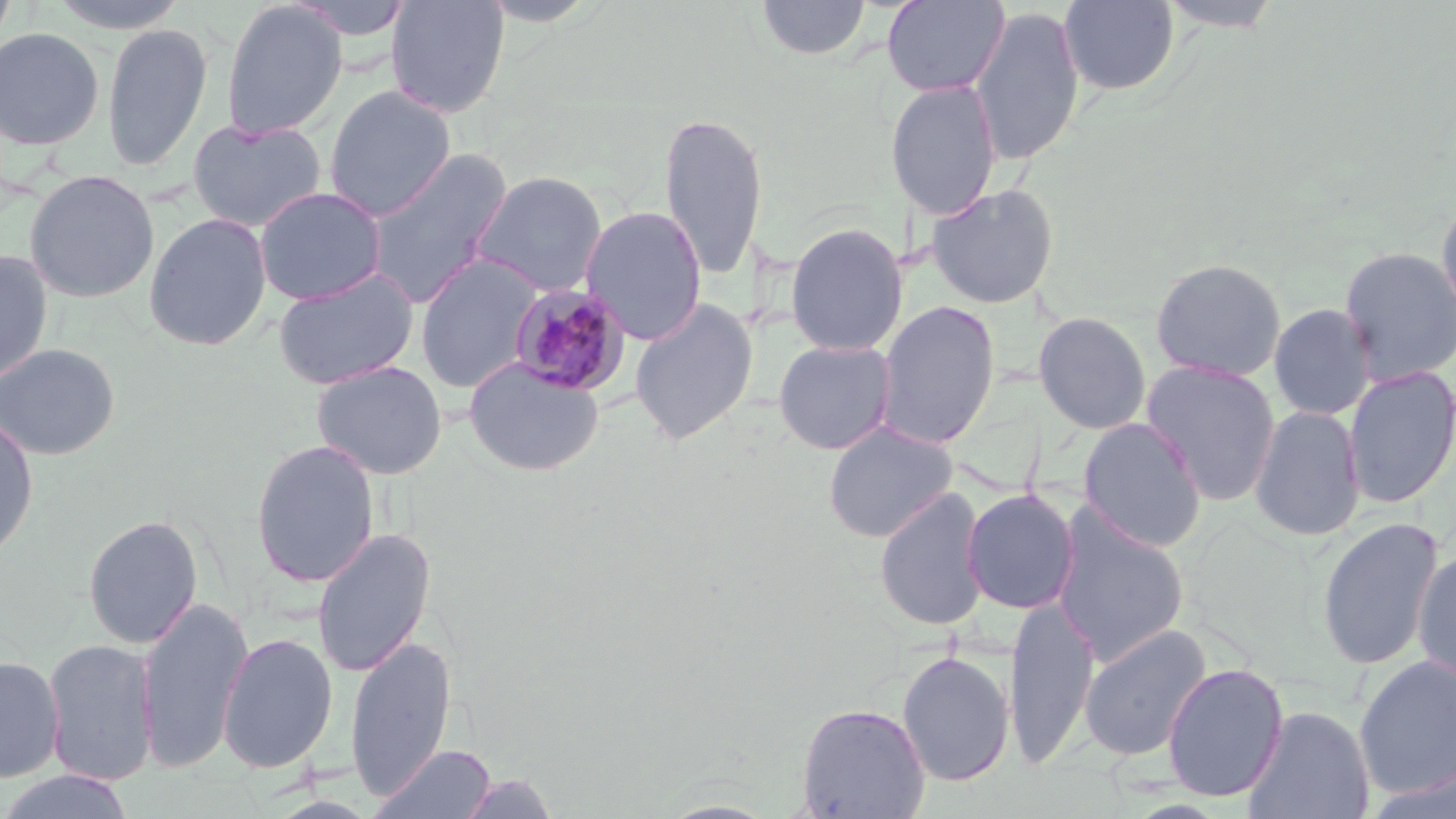

slide-level diagnosis = Plasmodium malariae
uninfected red blood cell locations = approximate bounding boxes as (x1, y1, x2, y2) in pixels: (0, 0, 18, 49), (46, 0, 190, 34), (287, 0, 416, 41), (385, 0, 510, 119), (756, 0, 871, 61), (881, 0, 1010, 97), (1155, 0, 1286, 32), (221, 1, 348, 140), (1058, 1, 1180, 95), (969, 6, 1085, 167), (102, 23, 212, 172), (0, 27, 104, 151), (885, 80, 1002, 221), (323, 85, 456, 221), (658, 111, 768, 282), (186, 118, 326, 233), (363, 148, 512, 307), (24, 169, 160, 303), (470, 170, 608, 298), (925, 183, 1060, 309), (253, 186, 387, 305), (1434, 196, 1456, 330), (580, 205, 708, 345), (144, 212, 272, 351), (785, 222, 908, 356), (1338, 245, 1456, 385), (0, 249, 54, 385), (415, 255, 542, 393), (1150, 257, 1287, 382), (272, 267, 419, 391), (629, 298, 759, 445), (876, 300, 1000, 450), (1269, 303, 1377, 420), (1033, 311, 1152, 435), (773, 339, 897, 454), (0, 343, 120, 460), (463, 356, 605, 477), (311, 359, 448, 480), (1141, 359, 1281, 506), (1342, 366, 1456, 509), (1249, 405, 1365, 542), (0, 414, 39, 560), (1077, 417, 1208, 553), (823, 421, 958, 543), (250, 439, 379, 588), (874, 485, 989, 632), (961, 488, 1080, 614), (1051, 506, 1189, 667), (82, 514, 203, 648), (1316, 516, 1444, 671), (311, 527, 436, 678), (1412, 549, 1456, 688), (136, 595, 253, 774), (1004, 598, 1100, 769), (1078, 623, 1212, 762), (217, 631, 338, 773), (345, 635, 455, 800), (43, 638, 159, 787), (896, 650, 1015, 786), (0, 654, 65, 783), (1353, 654, 1456, 800), (1161, 662, 1288, 802), (796, 702, 931, 818), (1241, 704, 1376, 819), (369, 743, 497, 819), (1363, 764, 1456, 819), (0, 770, 137, 819), (457, 773, 558, 818)
modality = light microscopy
stain = May-Grünwald-Giemsa
image size = 1456×819 pixels
preparation = thin blood film
Plasmodium malariae-infected red blood cell locations = approximate bounding boxes as (x1, y1, x2, y2) in pixels: (507, 283, 631, 398)
magnification = 1000x
field of view = one of a larger specimen